Assess the morphology of the red blood cells.
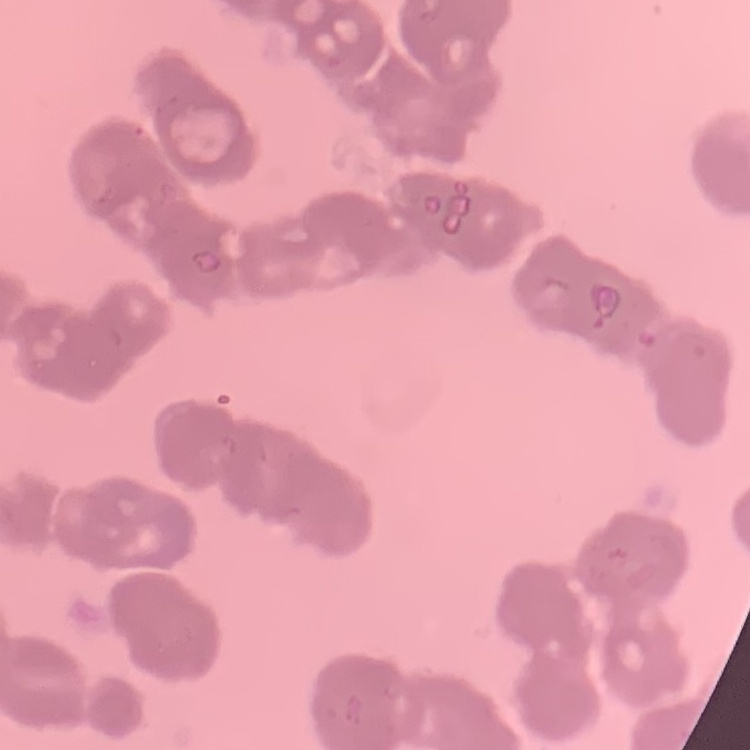

Rouleaux formation.

Summary:
  - Preparation: thin peripheral smear
  - Stain: Field's or Giemsa
  - Image type: one tile cut from a larger photomicrograph